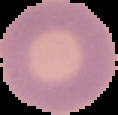
Summary:
  - Result: no Plasmodium parasites detected
  - Preparation: thin blood smear
  - Image type: segmented cell region with the area outside set to black
  - Image size: 118×115 pixels